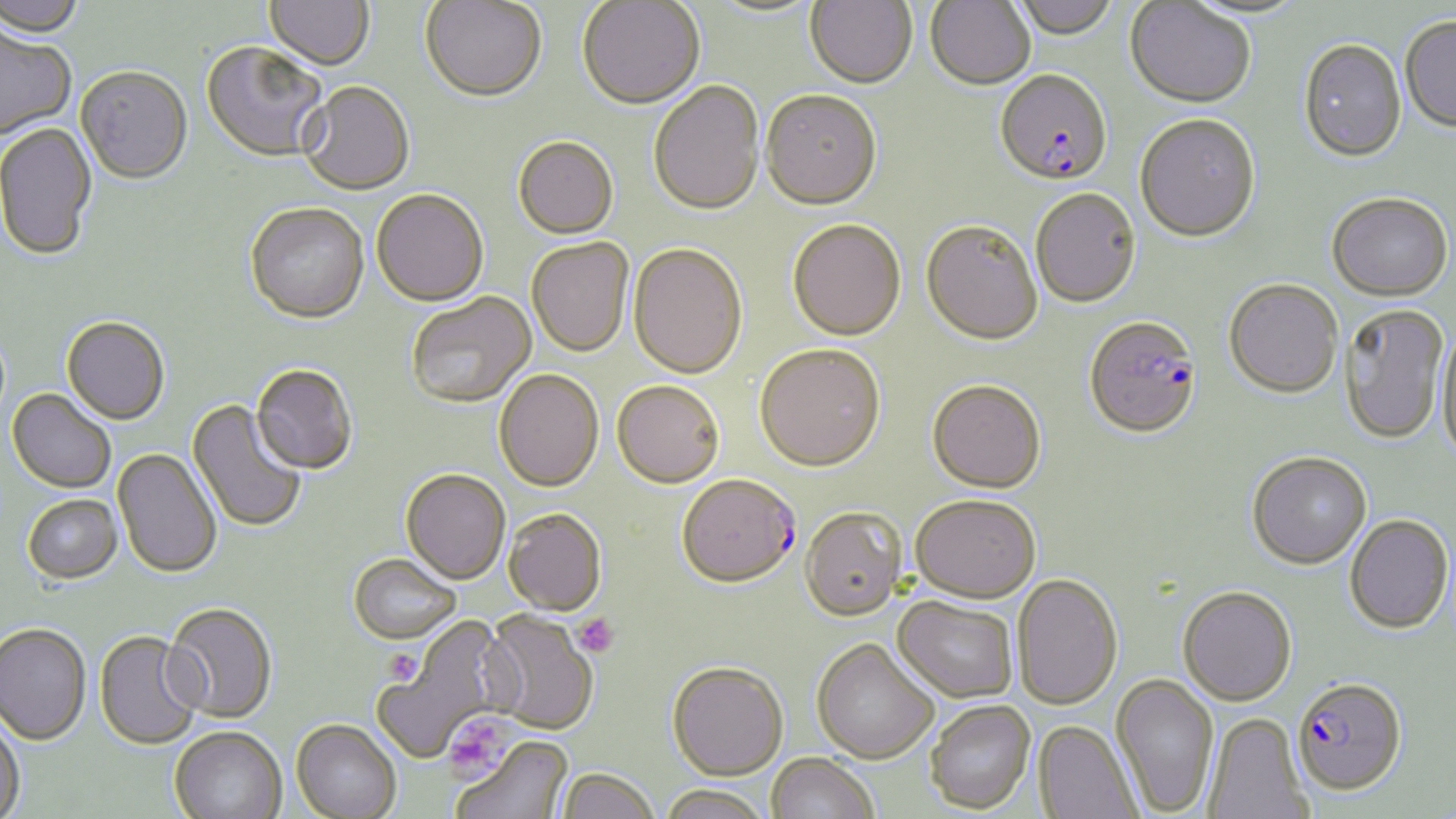
slide-level diagnosis = Plasmodium falciparum
modality = optical microscopy
magnification = 1000x
field of view = single
image size = 1456×819 pixels
uninfected red blood cell locations = approximate bounding boxes as (x1, y1, x2, y2) in pixels: (0, 0, 87, 37), (264, 0, 374, 71), (805, 0, 917, 90), (925, 0, 1035, 91), (1009, 0, 1120, 40), (420, 1, 546, 103), (577, 1, 705, 111), (1125, 2, 1256, 109), (1400, 16, 1456, 133), (0, 25, 76, 140), (1299, 40, 1407, 163), (201, 42, 330, 163), (76, 66, 193, 184), (298, 81, 415, 195), (648, 82, 765, 217), (760, 92, 882, 213), (1134, 115, 1261, 244), (0, 122, 97, 261), (513, 136, 619, 239), (371, 188, 489, 306), (1031, 189, 1141, 309), (1326, 193, 1453, 302), (245, 202, 369, 323), (787, 221, 906, 343), (920, 222, 1042, 348), (526, 238, 634, 357), (628, 245, 748, 380), (1223, 279, 1343, 400), (407, 292, 536, 408), (1339, 304, 1449, 445), (61, 316, 170, 425), (1436, 327, 1455, 463), (755, 346, 886, 474), (250, 363, 357, 475), (494, 369, 604, 492), (612, 380, 724, 489), (927, 381, 1046, 494), (7, 389, 116, 493), (187, 399, 307, 534), (113, 448, 222, 578), (1247, 453, 1372, 571), (401, 468, 510, 583), (22, 494, 122, 584), (910, 494, 1041, 604), (800, 508, 906, 621), (503, 509, 607, 616), (1344, 515, 1453, 636), (348, 552, 461, 644), (1012, 574, 1123, 711), (1177, 588, 1297, 708), (892, 596, 1018, 703), (163, 602, 278, 723), (482, 610, 599, 734), (376, 620, 512, 762), (0, 623, 91, 745), (94, 631, 203, 750), (811, 637, 939, 763), (666, 661, 787, 780), (1110, 674, 1219, 816), (926, 700, 1036, 815), (1203, 713, 1312, 819), (0, 715, 25, 819), (291, 719, 401, 819), (1033, 720, 1142, 819), (169, 727, 287, 819), (452, 736, 573, 819), (766, 753, 879, 819), (558, 768, 660, 819), (657, 784, 772, 819)
platelet locations = approximate bounding boxes as (x1, y1, x2, y2) in pixels: (573, 612, 620, 658), (382, 649, 422, 687), (444, 716, 510, 778)
preparation = thin blood smear
stain = May-Grünwald-Giemsa
Plasmodium falciparum-infected red blood cell locations = approximate bounding boxes as (x1, y1, x2, y2) in pixels: (995, 71, 1112, 187), (1084, 318, 1201, 440), (677, 473, 801, 587), (1292, 677, 1408, 797)